Assess this cell for malaria.
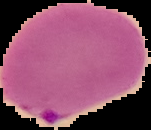
Parasitized.

Summary:
  - Preparation: thin blood smear
  - Image type: segmented cell region on a black background
  - Image size: 151×130 pixels